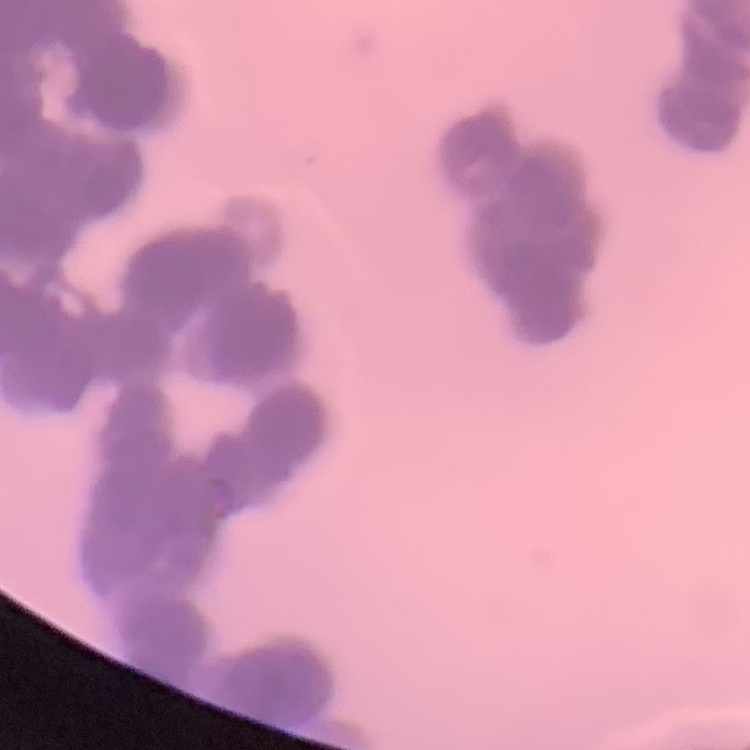

red blood cell morphology = rouleaux formation
stain = Field's or Giemsa
preparation = thin blood film
image type = one tile cut from a larger photomicrograph